Classify this cell by malaria status.
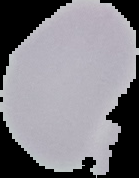

It is uninfected.

The area outside the segmented cell region is set to black. From a thin blood film. Image is 139×178 pixels.